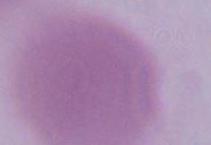
Summary:
  - Modality: photomicrograph
  - Identification: erythrocyte
  - Magnification: 1000x